Classify this cell by malaria status.
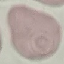
Uninfected.

Summary:
  - Image type: cell patch, automatically extracted from a larger field of view and resized to 64 × 64 pixels
  - Preparation: thin smear
  - Stain: Giemsa
  - Capture: smartphone camera at the microscope eyepiece